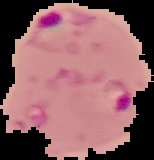

Summary:
  - Image size: 154×160 pixels
  - Preparation: thin blood smear
  - Image type: cell region segmented out of the field of view; surrounding area masked to black
  - Malaria status: parasitized